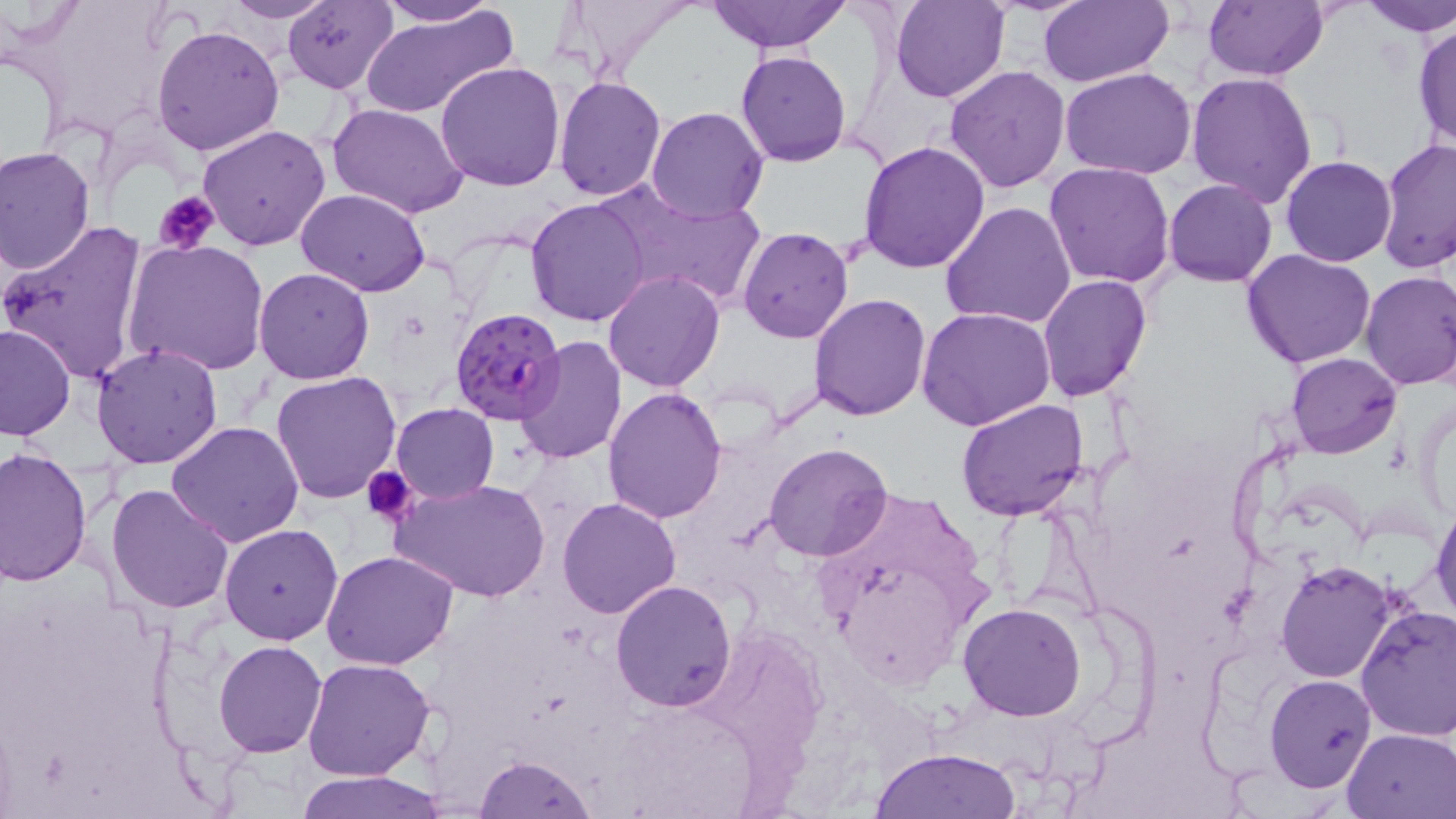

plasmodium_falciparum_infected_red_blood_cell_locations: 'approximate bounding boxes as (x1, y1, x2, y2) in pixels: (449, 307, 565, 428)'
slide_level_diagnosis: Plasmodium falciparum
preparation: thin blood smear
magnification: 1000x
field_of_view: one of a larger specimen
image_size: 1456×819 pixels
uninfected_red_blood_cell_locations: 'approximate bounding boxes as (x1, y1, x2, y2) in pixels: (374, 0, 504, 27), (559, 0, 702, 79), (706, 0, 851, 53), (891, 0, 1008, 104), (1038, 0, 1171, 88), (1202, 0, 1328, 81), (1355, 0, 1456, 37), (218, 1, 335, 23), (281, 1, 398, 93), (358, 7, 518, 119), (1412, 20, 1456, 152), (151, 23, 286, 157), (737, 50, 851, 166), (435, 61, 569, 191), (946, 65, 1073, 193), (1060, 67, 1199, 180), (1187, 73, 1319, 208), (554, 77, 668, 202), (328, 103, 470, 218), (646, 106, 768, 222), (198, 123, 331, 250), (1376, 137, 1456, 274), (857, 139, 990, 273), (1, 145, 97, 276), (1281, 155, 1397, 267), (1043, 161, 1175, 289), (1164, 179, 1278, 286), (594, 183, 766, 309), (296, 189, 432, 296), (525, 196, 652, 326), (940, 202, 1076, 331), (1, 222, 147, 382), (737, 227, 854, 343), (122, 238, 270, 377), (1241, 248, 1378, 369), (254, 267, 376, 384), (1359, 269, 1456, 391), (603, 271, 726, 392), (1037, 274, 1152, 401), (807, 294, 932, 421), (916, 307, 1058, 431), (1, 323, 76, 443), (516, 336, 629, 466), (91, 342, 223, 469), (1286, 352, 1401, 458), (271, 371, 404, 505), (603, 386, 728, 523), (954, 398, 1090, 522), (391, 402, 499, 504), (166, 421, 304, 547), (120, 442, 283, 597), (764, 442, 894, 561), (0, 447, 92, 586), (389, 477, 551, 602), (106, 482, 234, 615), (557, 496, 684, 620), (1431, 503, 1456, 625), (219, 523, 344, 645), (320, 550, 461, 671), (1276, 561, 1397, 683), (610, 581, 738, 711), (957, 601, 1088, 721), (1357, 606, 1456, 742), (213, 641, 326, 756), (302, 656, 436, 781), (1265, 674, 1376, 793), (1342, 727, 1456, 818), (869, 748, 1019, 819), (473, 755, 598, 818), (292, 771, 448, 819)'
stain: May-Grünwald-Giemsa
modality: light microscopy
platelet_locations: 'approximate bounding boxes as (x1, y1, x2, y2) in pixels: (155, 191, 218, 255), (362, 465, 418, 527)'